Classify this cell by malaria status.
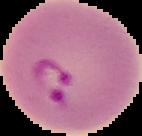
It is parasitized.

Summary:
  - Image type: segmented cell region on a black background
  - Preparation: thin blood smear
  - Image size: 142×136 pixels